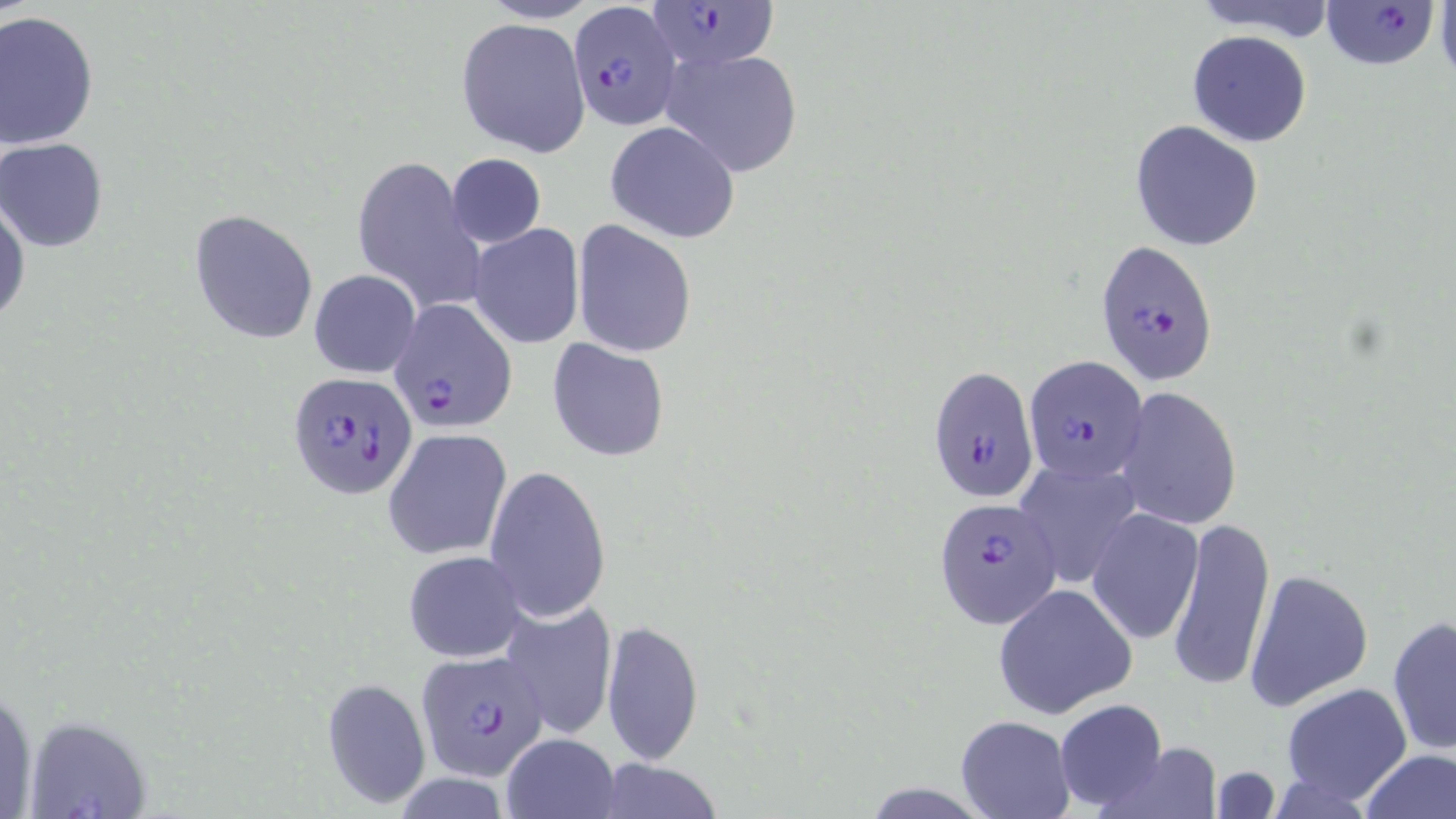

Summary:
  - Coordinate format: approximate bounding boxes as (x1,y1)-(x2,y2) corner pairs in pixels
  - Plasmodium falciparum-infected red blood cell locations: (569,1)-(682,130), (647,1)-(781,73), (1321,1)-(1441,71), (1094,239)-(1219,385), (390,299)-(517,432), (1023,356)-(1149,487), (927,363)-(1038,506), (288,370)-(416,498), (932,496)-(1060,628), (413,650)-(552,780)
  - Uninfected red blood cell locations: (1184,0)-(1337,38), (1434,1)-(1456,86), (0,11)-(100,150), (456,18)-(589,157), (1186,29)-(1312,147), (659,47)-(805,176), (1128,119)-(1265,252), (605,120)-(741,242), (0,138)-(108,252), (445,153)-(546,249), (351,161)-(484,312), (1,189)-(30,328), (188,209)-(319,344), (573,222)-(695,358), (468,225)-(585,349), (309,269)-(420,378), (547,338)-(670,462), (1114,385)-(1243,530), (382,427)-(512,560), (1013,457)-(1142,588), (484,466)-(611,626), (1087,507)-(1205,645), (1166,516)-(1274,693), (402,550)-(527,663), (1243,567)-(1375,711), (992,583)-(1136,719), (497,601)-(617,740), (1386,616)-(1455,757), (600,619)-(704,766), (321,678)-(430,808), (1281,683)-(1414,807), (1052,699)-(1171,812), (955,715)-(1075,819), (501,732)-(619,817), (1091,740)-(1225,819), (1359,748)-(1454,819), (586,758)-(726,819)
  - Slide-level diagnosis: Plasmodium falciparum
  - Modality: optical microscopy
  - Preparation: thin blood smear
  - Field of view: single
  - Stain: May-Grünwald-Giemsa
  - Magnification: 1000x
  - Image size: 1456×819 pixels